Assess this cell for malaria.
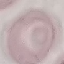
Uninfected.

image type = automatically extracted cell patch, resized to 64 × 64 pixels
stain = Giemsa
preparation = thin smear
capture = smartphone camera at the microscope eyepiece